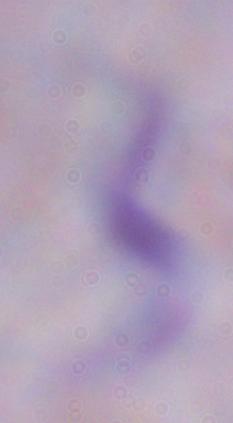

1000x magnification. A trypanosome is shown. Photomicrograph.